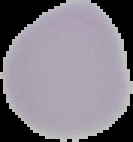 Result: negative for malaria parasites. Cell region segmented out of the field of view; the surrounding area is masked to black. From a thin blood smear. Image is 133×142 pixels.